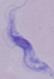

modality = photomicrograph
magnification = 1000x
identification = trypanosome